Point out every malaria parasite.
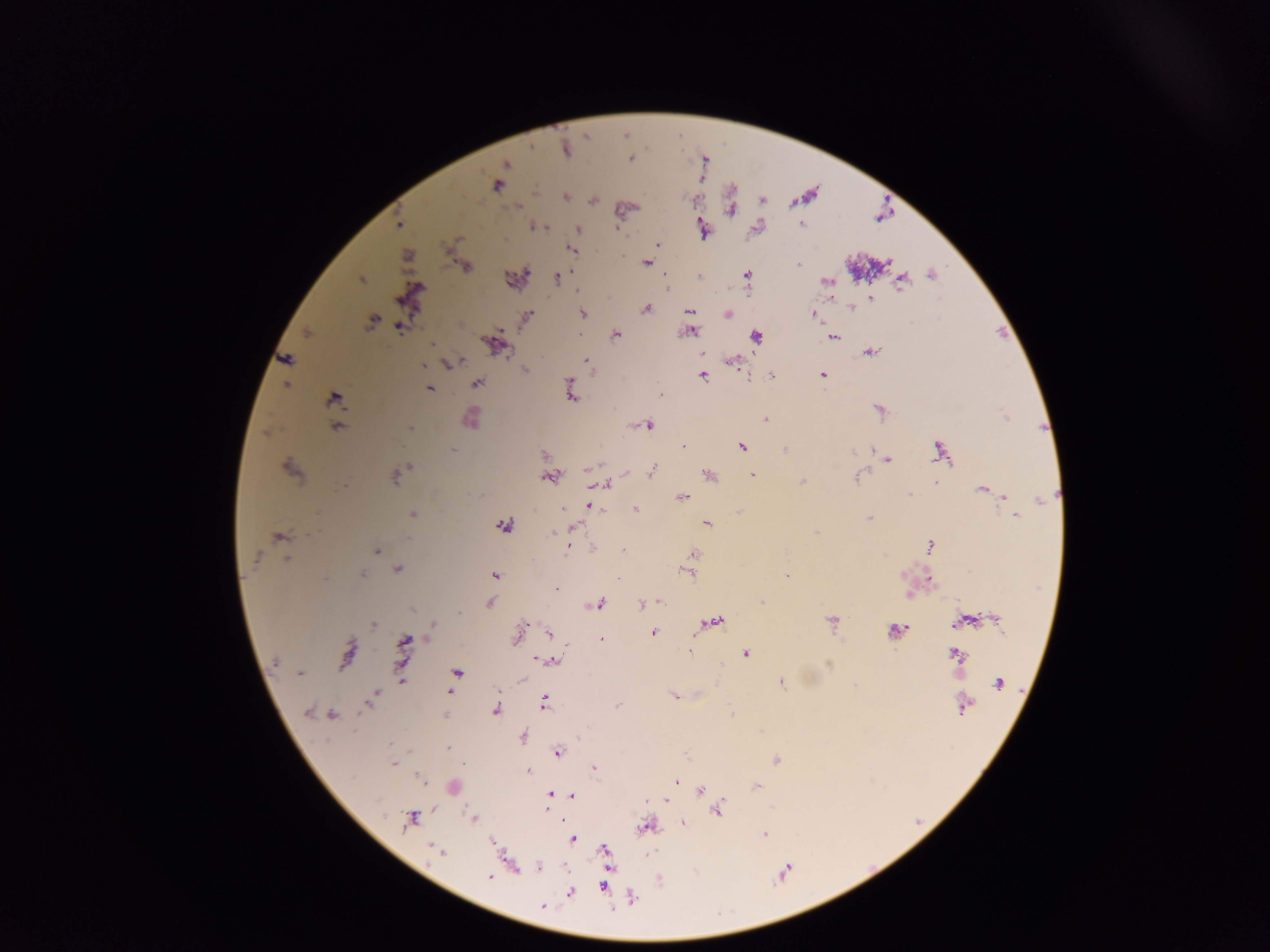
Approximate centers as x y in pixels.
Malaria parasites: 566 150; 630 158; 506 164; 497 185; 565 196; 399 224; 801 225; 542 227; 616 227; 702 227; 578 229; 657 244; 571 249; 407 255; 646 263; 797 265; 466 267; 747 275; 931 275; 700 277; 557 278; 361 279; 827 281; 901 281; 870 298; 831 299; 851 308; 647 309; 690 310; 584 313; 728 314; 812 315; 527 316; 372 321; 399 328; 691 331; 307 332; 616 335; 757 337; 833 337; 493 344; 871 352; 701 353; 286 358; 458 361; 586 361; 731 362; 449 364; 423 365; 525 369; 822 375; 703 376; 771 376; 477 383; 570 385; 286 386; 430 388; 570 394; 661 395; 334 399; 879 410; 472 418; 765 419; 648 426; 337 427; 410 429; 684 446; 741 447; 452 450; 784 450; 939 452; 852 453; 544 455; 888 460; 409 466; 290 469; 589 470; 652 470; 710 475; 753 475; 395 478; 549 479; 856 479; 803 482; 936 482; 605 484; 982 490; 910 494; 1004 497; 683 498; 1040 500; 590 506; 562 509; 636 509; 413 515; 1015 516; 870 518; 707 523; 504 525; 573 528; 552 532; 816 532; 278 537; 409 540; 930 545; 593 548; 377 551; 567 551; 623 551; 693 554; 255 558; 287 559; 398 570; 687 573; 363 574; 494 575; 787 576; 557 588; 908 595; 660 602; 762 602; 490 603; 599 604; 641 604; 411 610; 459 613; 997 620; 831 621; 961 621; 715 622; 373 625; 433 627; 896 630; 653 633; 549 634; 518 635; 428 636; 601 639; 404 641; 690 651; 746 653; 347 654; 955 654; 541 660; 552 661; 276 662; 829 665; 300 673; 457 673; 521 680; 401 681; 781 683; 998 684; 449 693; 674 696; 373 697; 544 702; 369 704; 965 705; 617 706; 496 710; 307 712; 732 714; 332 715; 446 716; 523 737; 448 747; 558 753; 776 760; 393 764; 594 769; 527 770; 420 779; 676 782; 757 787; 701 791; 550 795; 572 796; 665 800; 718 811; 474 818; 411 820; 683 823; 645 827; 764 834; 572 839; 492 842; 437 850; 604 850; 538 867; 488 877; 602 886; 570 893; 632 898; 542 906.

Leukocyte locations: 451 787. Image is 1270×952 pixels. Thick blood smear. Collected in Ghana. Single field of view. Photographed through a microscope with a mobile-phone camera.